Name the cell type shown.
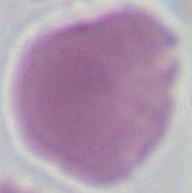
This is an erythrocyte.

{
  "modality": "photomicrograph",
  "magnification": "1000x"
}